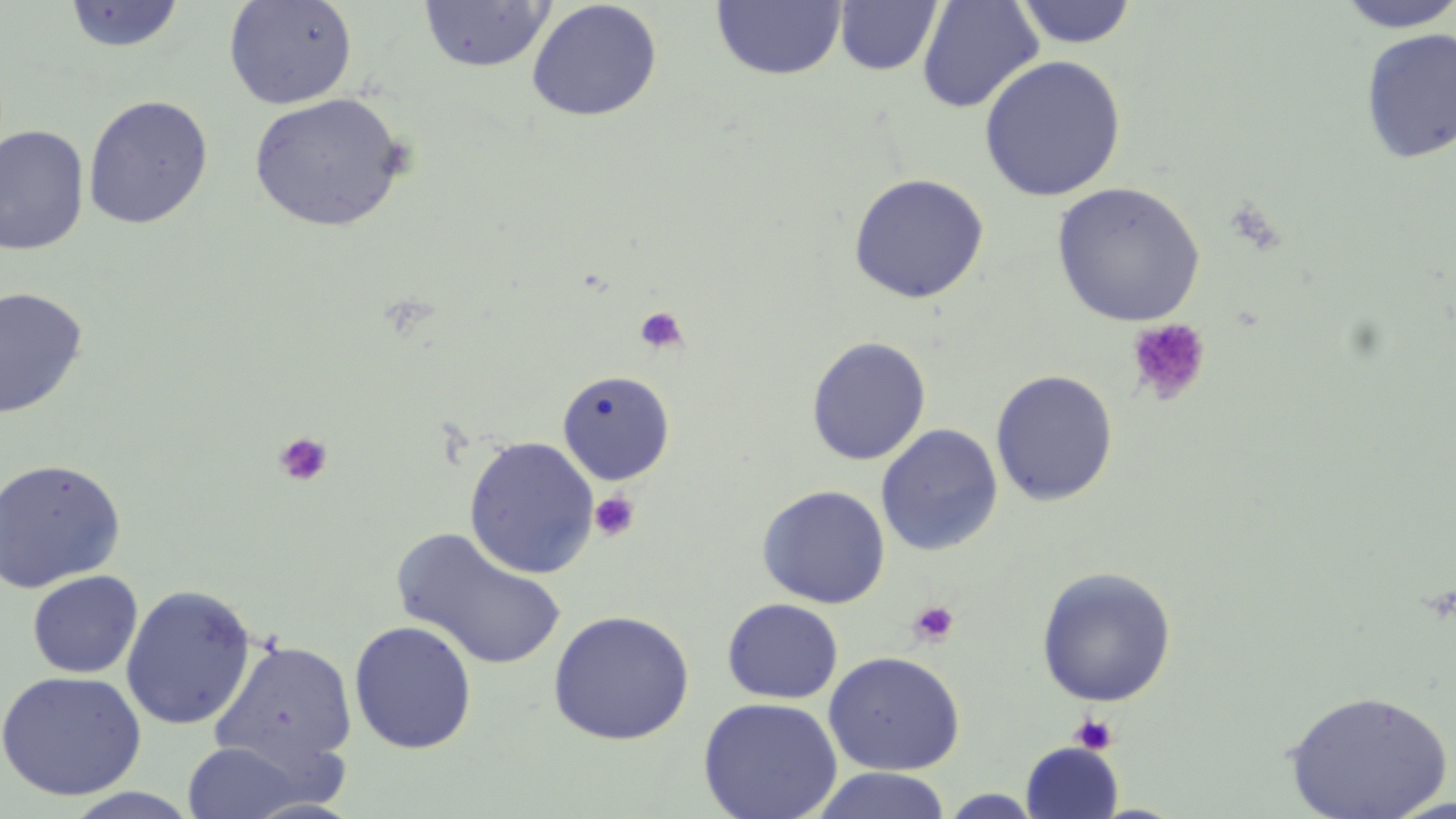
Approximate bounding boxes as [x1, y1, x2, y2] in pixels. Uninfected red blood cell locations: [223, 0, 358, 110], [711, 0, 846, 80], [833, 0, 943, 76], [1012, 0, 1139, 48], [1333, 0, 1456, 33], [63, 1, 186, 53], [418, 1, 554, 73], [526, 1, 663, 122], [916, 1, 1044, 114], [1359, 28, 1456, 164], [979, 55, 1127, 201], [248, 92, 409, 233], [82, 94, 214, 229], [0, 125, 90, 255], [847, 172, 989, 304], [1051, 182, 1205, 327], [0, 286, 89, 420], [806, 336, 931, 466], [556, 369, 675, 485], [990, 369, 1118, 506], [876, 423, 1004, 557], [463, 435, 599, 579], [0, 458, 126, 594], [756, 484, 890, 608], [393, 527, 568, 671], [1036, 566, 1177, 707], [27, 570, 143, 678], [15, 572, 146, 779], [120, 584, 257, 731], [722, 598, 843, 704], [548, 609, 695, 746], [349, 620, 478, 754], [211, 638, 357, 770], [823, 651, 965, 775], [0, 670, 147, 801], [1284, 689, 1453, 819], [698, 696, 842, 819], [182, 741, 309, 818], [1021, 742, 1123, 818], [809, 768, 952, 819], [61, 788, 204, 818], [939, 790, 1044, 818]. Platelet locations: [634, 306, 689, 354], [1126, 318, 1211, 407], [273, 431, 334, 487], [590, 491, 641, 541], [907, 600, 960, 647], [1069, 712, 1118, 755]. Slide-level diagnosis: no evidence of blood parasites. Optical microscopy. Single field of view. Thin blood smear. Captured at 1000x magnification. Image is 1456×819 pixels. May-Grünwald-Giemsa-stained preparation.